Classify this cell by malaria status.
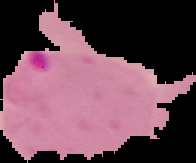
Parasitized.

{
  "image_type": "segmented cell region on a black background",
  "image_size": "196×163 pixels",
  "preparation": "thin blood smear"
}